Comment on the morphology of the erythrocytes.
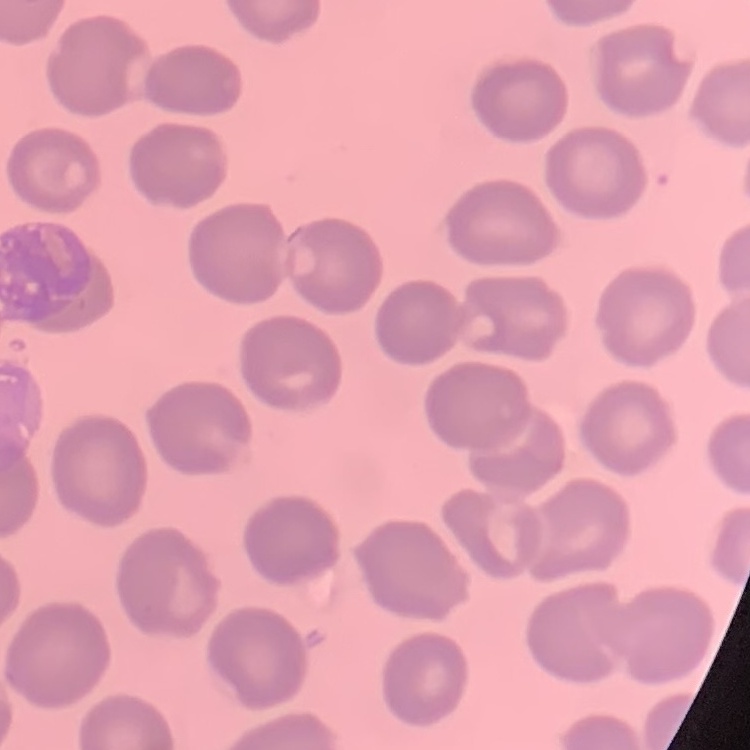
They show no rouleaux formation.

Summary:
  - Preparation: thin blood film
  - Stain: Field's or Giemsa
  - Image type: one tile cut from a larger photomicrograph